Classify this cell by malaria status.
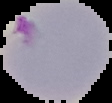

It is parasitized.

preparation: thin blood smear
image_size: 112×103 pixels
image_type: segmented cell region on a black background